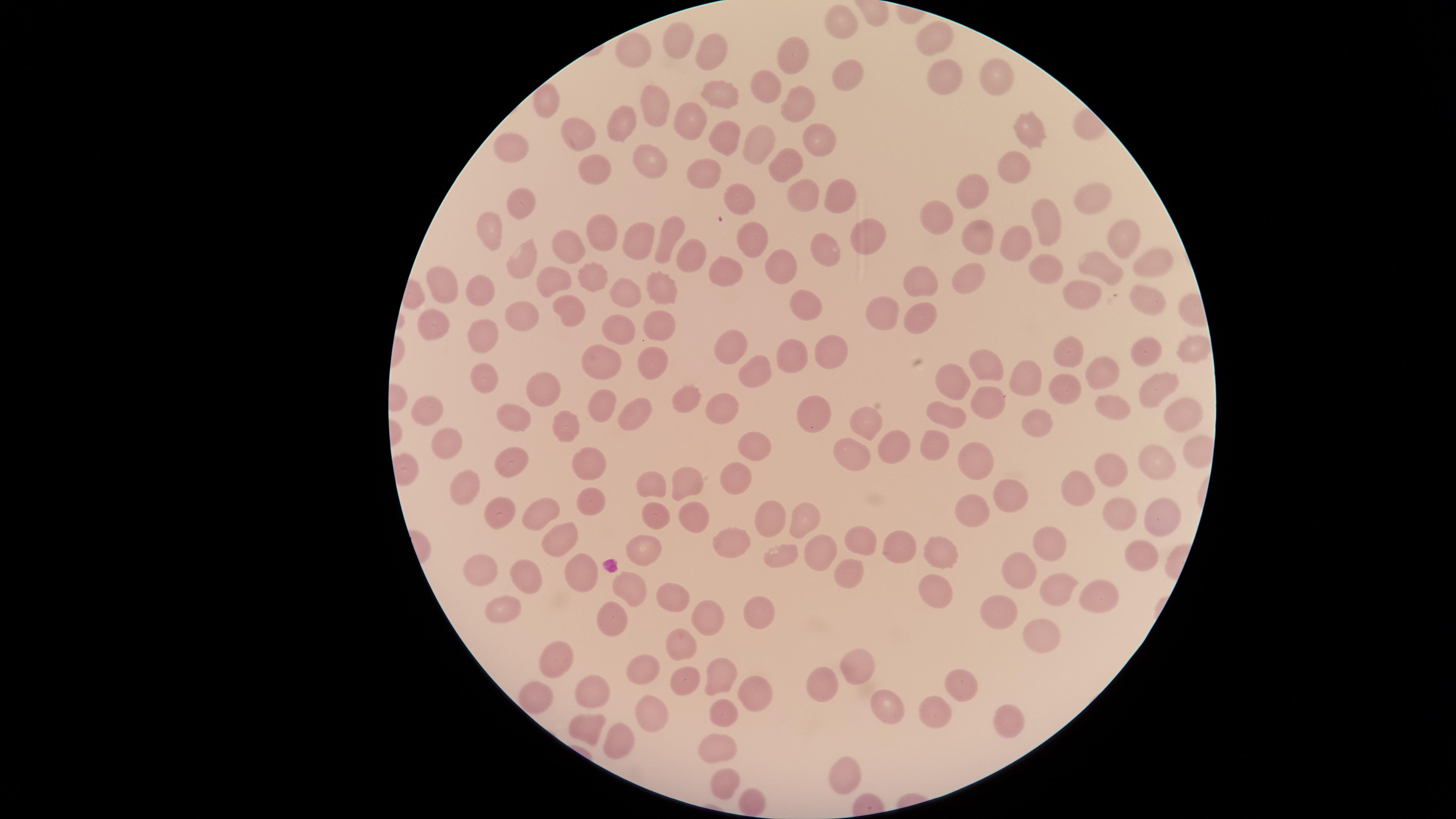

{
  "preparation": "thin blood smear",
  "field_of_view": "single",
  "visible_region": "circular",
  "capture": "smartphone photograph through the microscope eyepiece",
  "stain": "Giemsa",
  "uninfected_red_blood_cells": "approximate marker points as (x, y) in pixels: (838, 19), (932, 31), (709, 42), (676, 43), (631, 52), (792, 53), (996, 73), (851, 75), (945, 77), (768, 83), (721, 94), (546, 96), (797, 100), (652, 105), (691, 121), (617, 127), (1024, 129), (571, 131), (819, 133), (726, 136), (760, 139), (508, 151), (784, 163), (650, 165), (1010, 165), (594, 169), (706, 169), (977, 192), (794, 194), (842, 194), (736, 195), (1088, 195), (520, 200), (931, 212), (1040, 221), (491, 227), (599, 230), (984, 230), (860, 233), (635, 234), (747, 235), (1125, 237), (1017, 239), (665, 240), (569, 241), (828, 247), (690, 254), (522, 257), (1149, 260), (775, 264), (1045, 265), (1099, 266), (589, 270), (726, 274), (555, 278), (964, 279), (441, 280), (923, 284), (656, 285), (622, 286), (480, 290), (1081, 295), (804, 300), (1151, 301), (568, 306), (517, 315), (882, 315), (921, 318), (657, 323), (436, 326), (607, 335), (481, 336), (829, 345), (733, 346), (1190, 350), (1060, 353), (1146, 354), (792, 358), (651, 362), (984, 363), (604, 364), (746, 368), (1096, 369), (1026, 375), (484, 377), (952, 377), (1157, 386), (542, 387), (1064, 392), (681, 394), (993, 403), (728, 405), (438, 406), (607, 406), (1115, 409), (1174, 410), (948, 411), (815, 414), (632, 416), (514, 418), (1032, 419), (858, 421), (572, 425), (932, 439), (888, 440), (448, 441), (754, 445), (850, 452), (977, 457), (514, 458), (1147, 459), (589, 463), (1108, 471), (735, 476), (466, 480), (689, 481), (654, 486), (1078, 490), (1005, 493), (588, 499), (1109, 506), (499, 510), (534, 511), (647, 511), (1157, 512), (691, 514), (804, 516), (976, 516), (772, 519), (555, 535), (1049, 537), (899, 541), (735, 542), (858, 542), (646, 546), (941, 549), (819, 550), (780, 552), (1137, 556), (474, 560), (1020, 570), (583, 572), (851, 572), (525, 578), (930, 581), (1061, 584), (631, 586), (671, 593), (1091, 597), (506, 602), (763, 613), (1000, 615), (613, 620), (713, 620), (1036, 632), (685, 644), (560, 650), (643, 666), (852, 668), (719, 674), (685, 677), (823, 683), (963, 685), (595, 687), (749, 690), (536, 693), (929, 706), (879, 709), (653, 711), (726, 718), (1008, 718), (593, 729), (621, 739), (716, 749), (843, 772), (729, 781), (751, 800)",
  "image_size": "1456×819 pixels",
  "presence": "no malaria parasites identified"
}